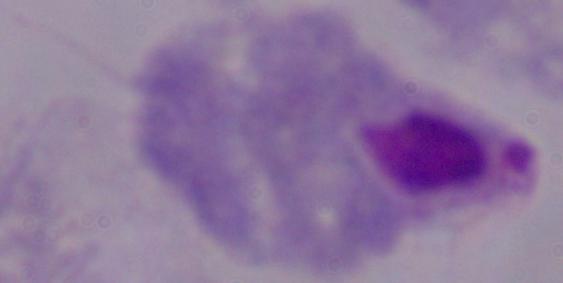 Captured at 1000x magnification. Photomicrograph. A trichomonad is shown.